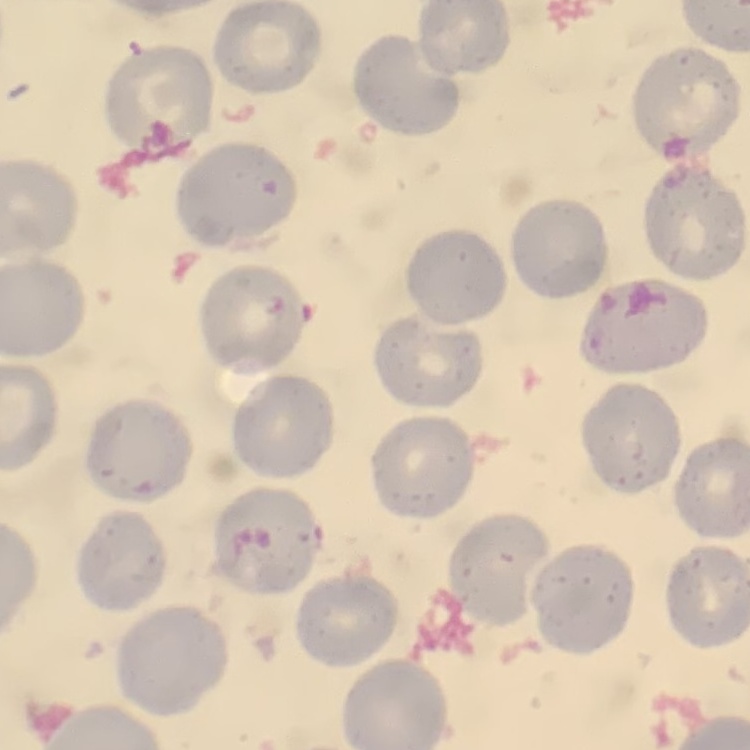

Summary:
  - Erythrocyte morphology: no rouleaux formation
  - Stain: Field's or Giemsa
  - Image type: one tile cut from a larger photomicrograph
  - Preparation: thin blood film